Assess this cell for malaria.
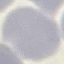
It is uninfected.

capture = smartphone through the microscope eyepiece
image type = automatically extracted cell patch, resized to 64 × 64 pixels
preparation = thin smear
stain = Giemsa